Comment on the morphology of the erythrocytes.
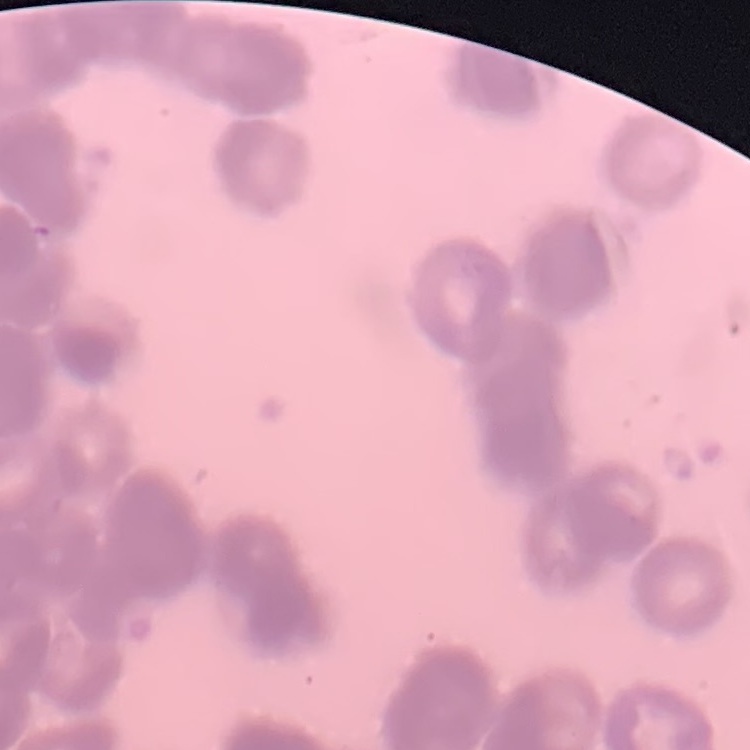

Rouleaux formation.

Thin peripheral smear. Field's or Giemsa stain. Square crop of a larger photomicrograph.